Locate every leukocyte (white blood cell).
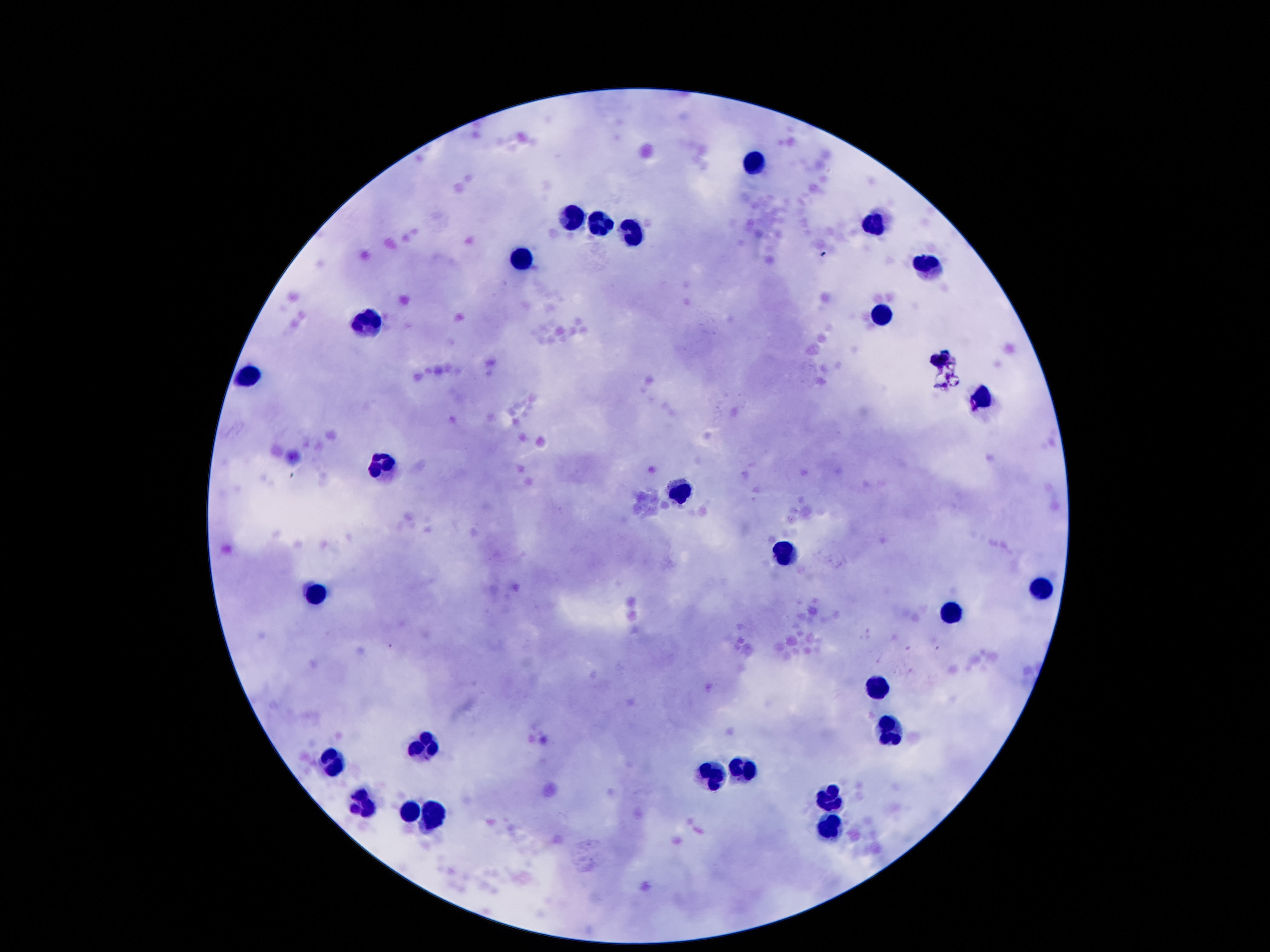

Approximate centers as [x, y] in pixels.
Leukocytes: [756, 163], [576, 216], [603, 227], [875, 227], [632, 236], [523, 258], [928, 265], [882, 313], [377, 317], [941, 359], [249, 375], [986, 399], [380, 463], [683, 488], [786, 554], [1041, 589], [316, 596], [957, 609], [875, 684], [890, 731], [422, 744], [335, 764], [749, 771], [716, 777], [833, 793], [362, 808], [411, 813], [433, 815], [829, 830].

Single field of view. 100x magnification. Photographed through the microscope eyepiece with a smartphone camera. Patient malaria status: not infected. Image is 1270×952 pixels. Giemsa-stained preparation. Thick blood film.